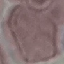
Result: no malaria parasites detected. Acquired by smartphone through the microscope eyepiece. Giemsa stain. Cell patch, automatically extracted from a larger field of view and resized to 64 × 64 pixels. Thin smear of blood.